Assess the morphology of the erythrocytes.
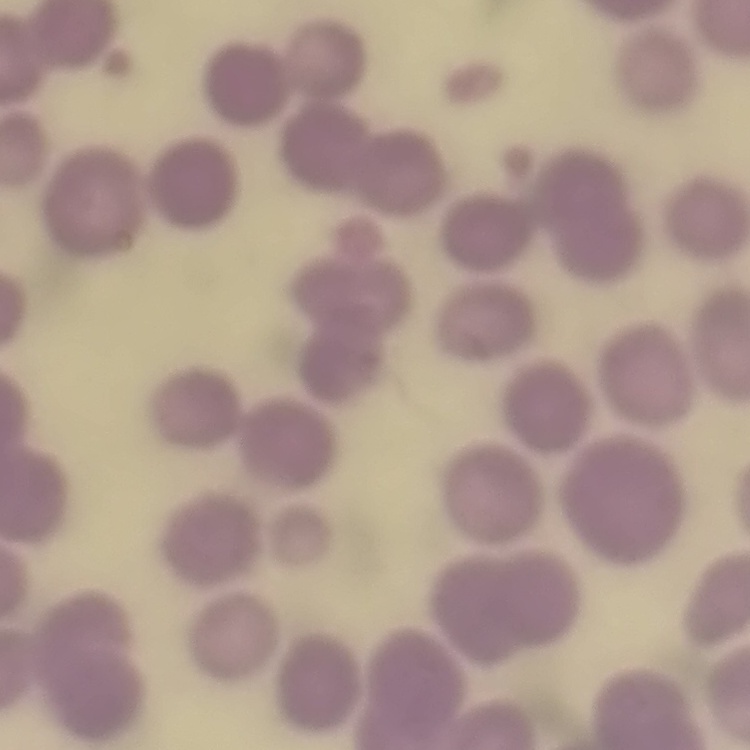

No rouleaux formation.

stain: Field's or Giemsa
image_type: one tile cut from a larger photomicrograph
preparation: thin blood smear